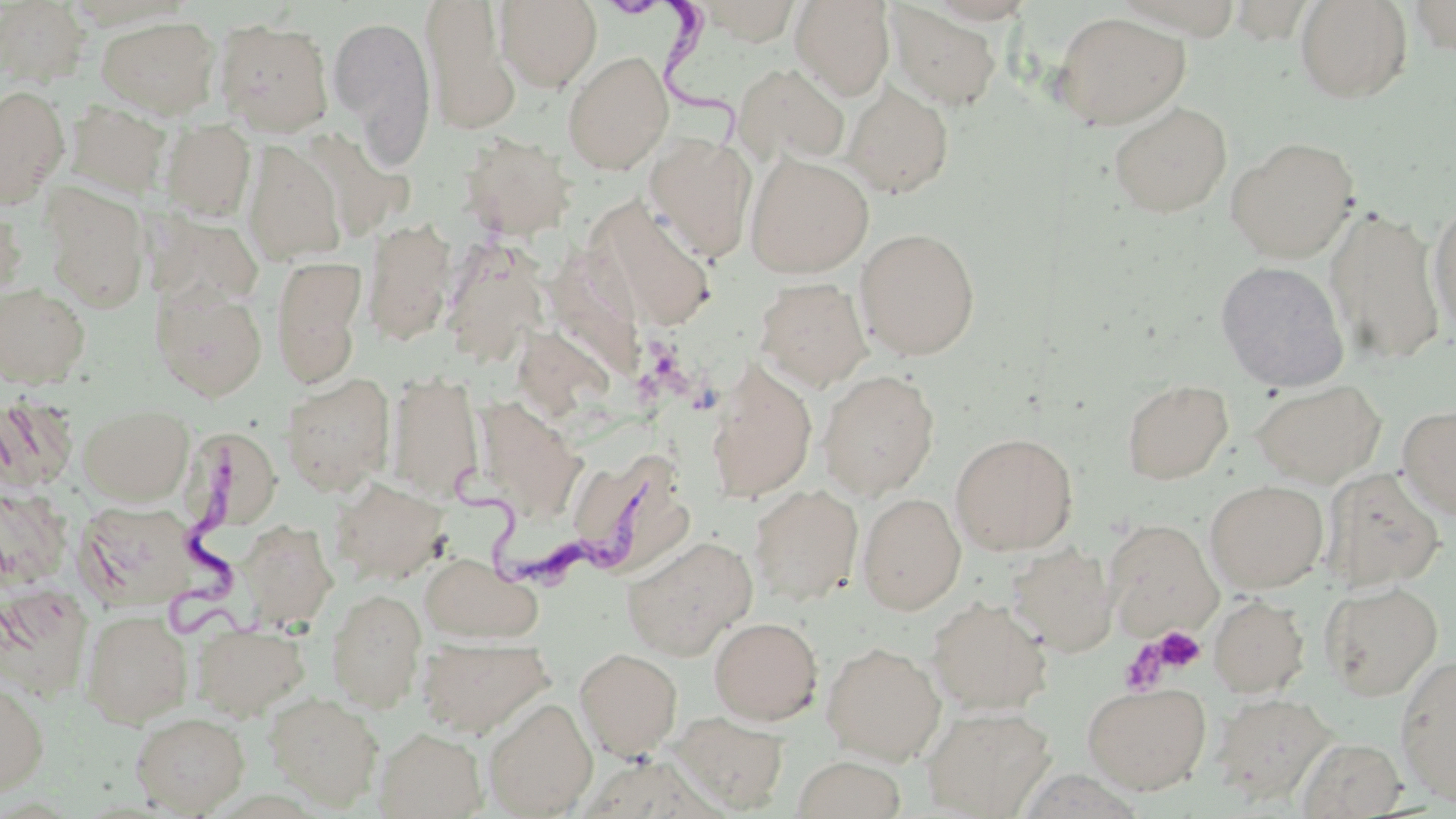

Approximate bounding boxes as (x1, y1, x2, y2) in pixels. Uninfected red blood cell locations: (494, 0, 601, 91), (699, 0, 802, 44), (1408, 0, 1456, 57), (0, 1, 90, 86), (789, 1, 895, 101), (1114, 1, 1240, 36), (1227, 1, 1318, 43), (1294, 1, 1413, 104), (420, 2, 520, 135), (886, 3, 1003, 111), (1052, 12, 1190, 130), (328, 14, 436, 162), (96, 15, 220, 119), (213, 19, 334, 136), (563, 50, 674, 176), (731, 61, 850, 165), (842, 80, 955, 198), (0, 85, 69, 207), (65, 99, 171, 198), (1108, 102, 1232, 217), (161, 119, 255, 221), (458, 132, 577, 241), (644, 133, 757, 262), (1225, 136, 1360, 263), (242, 140, 346, 266), (744, 151, 874, 278), (41, 184, 150, 312), (1427, 199, 1456, 334), (593, 201, 719, 330), (0, 202, 26, 304), (1325, 206, 1446, 367), (151, 211, 264, 310), (362, 218, 457, 346), (855, 227, 980, 360), (442, 242, 550, 364), (271, 256, 367, 388), (1215, 260, 1349, 392), (754, 277, 872, 392), (0, 281, 92, 388), (151, 285, 267, 401), (705, 360, 818, 504), (818, 369, 940, 499), (385, 372, 483, 501), (280, 373, 395, 495), (1121, 378, 1233, 484), (1251, 379, 1386, 487), (80, 405, 193, 504), (1397, 405, 1456, 519), (181, 422, 275, 532), (950, 432, 1078, 555), (568, 448, 689, 575), (1322, 467, 1446, 592), (328, 474, 451, 586), (1205, 480, 1328, 593), (749, 484, 864, 607), (857, 493, 966, 614), (75, 500, 202, 610), (1103, 518, 1222, 639), (238, 520, 338, 630), (620, 535, 758, 660), (1006, 543, 1118, 657), (420, 554, 541, 644), (1321, 581, 1443, 700), (0, 583, 92, 700), (326, 588, 427, 712), (1209, 594, 1310, 698), (926, 596, 1052, 715), (81, 609, 192, 727), (709, 616, 823, 725), (192, 622, 309, 719), (418, 637, 552, 738), (821, 641, 945, 764), (574, 647, 683, 758), (1394, 654, 1456, 805), (0, 677, 49, 796), (1082, 682, 1211, 794), (264, 691, 384, 809), (1212, 692, 1335, 804), (483, 697, 598, 817), (922, 705, 1055, 817), (130, 711, 250, 815), (670, 712, 790, 813), (374, 726, 487, 818), (1297, 737, 1407, 817), (793, 756, 906, 819). Platelet locations: (1152, 625, 1205, 673), (1119, 640, 1170, 696). Trypanosoma brucei locations: (614, 0, 752, 145), (169, 444, 252, 640), (450, 466, 661, 596). Slide-level diagnosis: Trypanosoma brucei. Light microscopy. Captured at 1000x magnification. One field of a larger specimen. Image is 1456×819 pixels. May-Grünwald-Giemsa-stained preparation. Thin blood smear.